Classify this cell by malaria status.
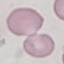

Uninfected.

Giemsa stain. Cell patch, automatically extracted from a larger field of view and resized to 64 × 64 pixels. Thin blood film. Photographed with a smartphone camera at the microscope eyepiece.